State the blood parasite species.
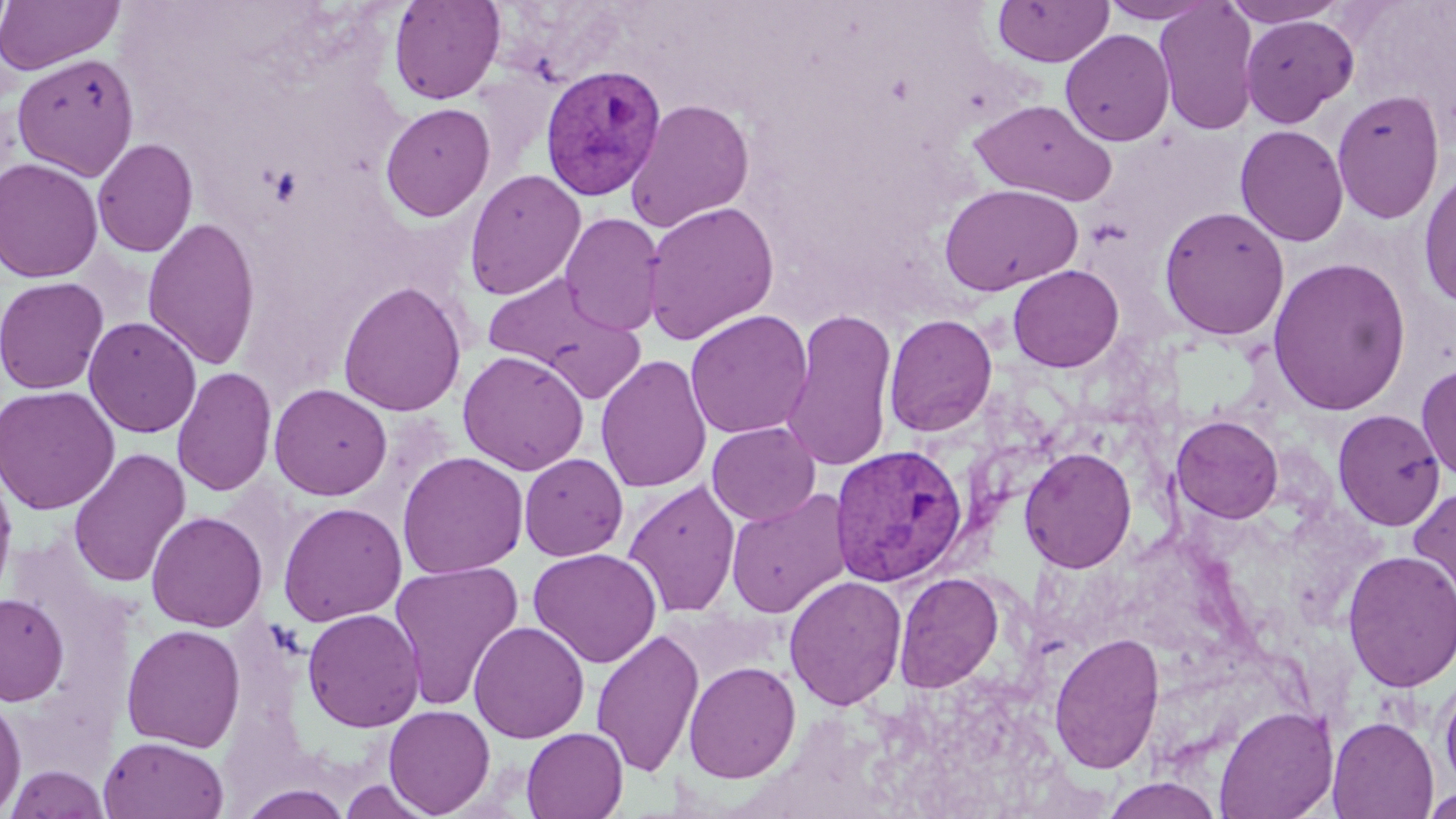

Plasmodium vivax.

Summary:
  - Coordinate format: approximate bounding boxes as (x1,y1)-(x2,y2) corner pairs in pixels
  - Plasmodium vivax-infected red blood cell locations: (540,64)-(668,203), (828,443)-(968,587)
  - Uninfected red blood cell locations: (0,0)-(124,75), (388,0)-(505,104), (993,0)-(1113,67), (1154,0)-(1260,136), (1222,0)-(1349,26), (1099,1)-(1217,24), (1240,14)-(1359,127), (1060,29)-(1175,147), (12,53)-(139,179), (1331,88)-(1446,225), (625,99)-(755,232), (968,99)-(1118,206), (379,102)-(496,222), (1234,124)-(1349,247), (92,138)-(198,258), (0,157)-(104,283), (1417,167)-(1456,310), (464,169)-(586,300), (939,183)-(1083,296), (641,200)-(779,346), (1158,205)-(1290,340), (559,212)-(665,337), (142,217)-(261,370), (1267,257)-(1411,416), (1008,265)-(1124,372), (481,270)-(645,395), (0,276)-(109,395), (337,280)-(468,417), (780,308)-(899,473), (685,310)-(813,439), (883,314)-(998,437), (83,316)-(202,438), (457,349)-(590,476), (595,354)-(713,494), (1416,364)-(1456,484), (171,365)-(277,497), (268,383)-(393,500), (0,386)-(120,514), (1333,409)-(1446,531), (1171,416)-(1283,523), (706,422)-(820,525), (1019,446)-(1138,573), (67,448)-(191,588), (396,451)-(529,580), (519,453)-(628,561), (0,467)-(18,608), (623,480)-(741,617), (1408,485)-(1456,611), (725,489)-(851,619), (277,502)-(407,626), (145,511)-(268,633), (528,547)-(663,668), (1341,549)-(1456,693), (389,560)-(524,711), (893,571)-(1005,693), (784,575)-(907,711), (0,593)-(69,705), (302,608)-(424,732), (468,621)-(590,743), (121,623)-(247,752), (591,628)-(705,778), (1049,632)-(1165,775), (683,660)-(802,783), (1437,670)-(1456,796), (0,694)-(27,816), (383,704)-(496,817), (1213,705)-(1339,819), (1327,716)-(1439,818), (521,727)-(628,819), (98,735)-(229,819), (5,765)-(110,818), (1100,777)-(1223,819), (237,783)-(355,819), (1421,788)-(1456,818)
  - Preparation: thin blood smear
  - Image size: 1456×819 pixels
  - Modality: light microscopy
  - Stain: May-Grünwald-Giemsa
  - Magnification: 1000x
  - Field of view: one of a larger specimen